Outline each uninfected red blood cell.
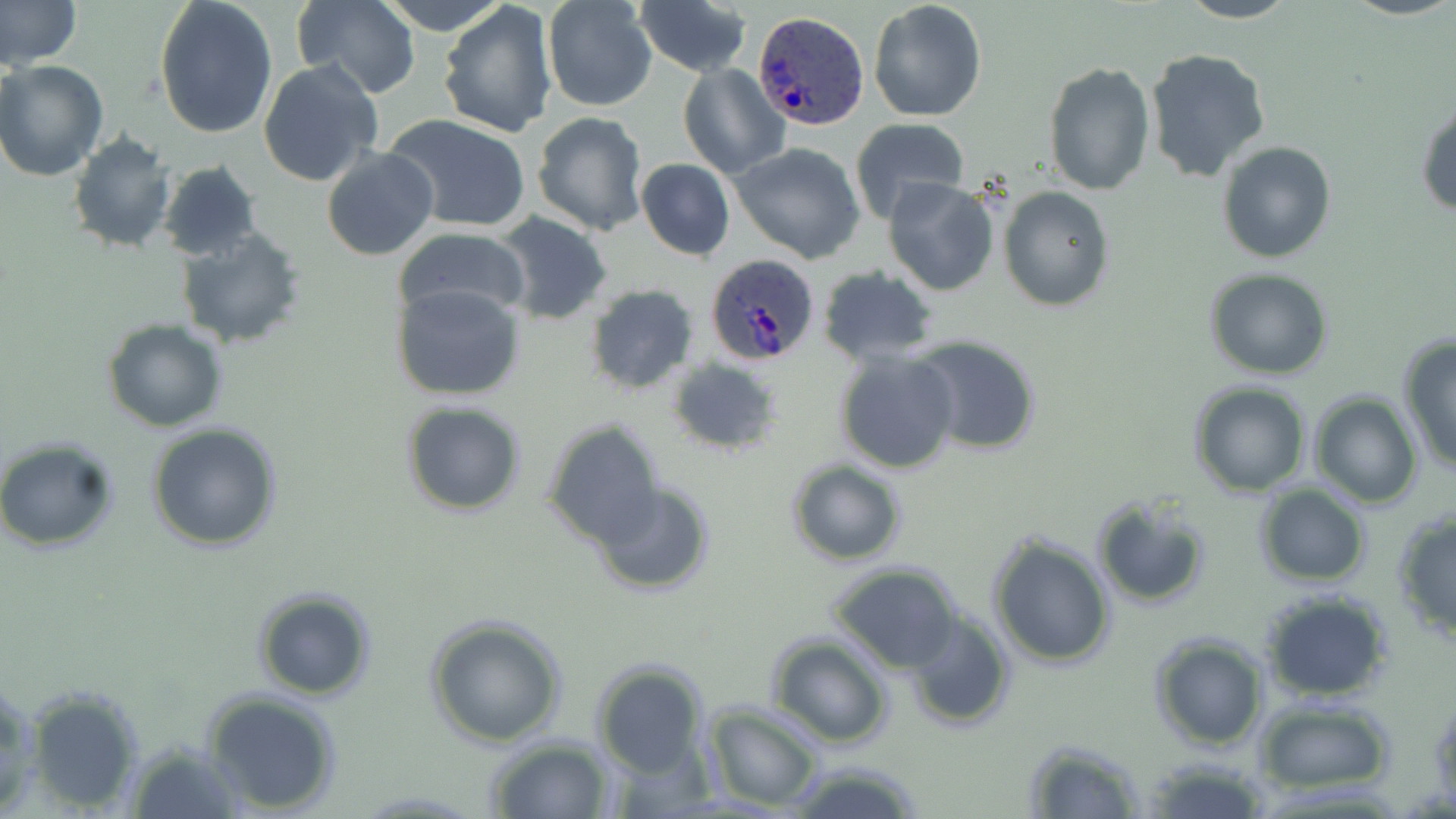

Approximate bounding boxes as (x1, y1, x2, y2) in pixels.
Uninfected red blood cells: (0, 0, 80, 70), (152, 0, 277, 140), (290, 0, 420, 99), (381, 0, 508, 34), (541, 0, 659, 112), (633, 0, 753, 77), (869, 0, 987, 123), (1178, 0, 1298, 23), (438, 2, 561, 139), (1144, 48, 1271, 182), (0, 59, 108, 180), (257, 61, 382, 187), (1043, 61, 1155, 195), (678, 63, 791, 178), (1416, 102, 1456, 219), (532, 111, 649, 237), (384, 114, 532, 235), (849, 118, 970, 223), (66, 132, 176, 255), (1217, 140, 1335, 263), (730, 143, 866, 263), (321, 146, 440, 262), (636, 159, 735, 261), (156, 161, 264, 263), (882, 177, 1000, 296), (998, 186, 1115, 312), (492, 211, 614, 325), (392, 226, 530, 325), (176, 228, 306, 347), (815, 265, 940, 367), (1205, 270, 1333, 379), (391, 282, 525, 401), (583, 283, 699, 395), (102, 319, 228, 431), (907, 336, 1042, 456), (1399, 337, 1456, 472), (833, 348, 961, 475), (665, 358, 784, 456), (1189, 381, 1310, 496), (1309, 393, 1423, 508), (400, 400, 526, 516), (542, 419, 667, 547), (147, 423, 282, 551), (0, 436, 120, 553), (786, 460, 907, 566), (589, 480, 716, 597), (1254, 483, 1371, 587), (1090, 496, 1211, 610), (1391, 508, 1456, 645), (986, 533, 1114, 668), (828, 564, 964, 672), (252, 588, 376, 700), (1262, 592, 1392, 702), (904, 611, 1014, 731), (423, 615, 568, 747), (1150, 633, 1266, 750), (766, 634, 893, 747), (589, 659, 709, 778), (0, 675, 37, 815), (20, 686, 144, 811), (203, 689, 340, 815), (1428, 691, 1456, 805), (1257, 702, 1390, 792), (704, 705, 824, 811), (484, 737, 613, 818), (1022, 738, 1144, 818), (121, 741, 246, 819), (1142, 757, 1274, 819), (782, 760, 927, 819).

Summary:
  - Plasmodium ovale-infected red blood cell locations: (754, 11, 868, 129), (701, 254, 823, 365)
  - Slide-level diagnosis: Plasmodium ovale
  - Modality: optical microscopy
  - Field of view: single
  - Image size: 1456×819 pixels
  - Stain: May-Grünwald-Giemsa
  - Magnification: 1000x
  - Preparation: thin blood smear